Assess the morphology of the erythrocytes.
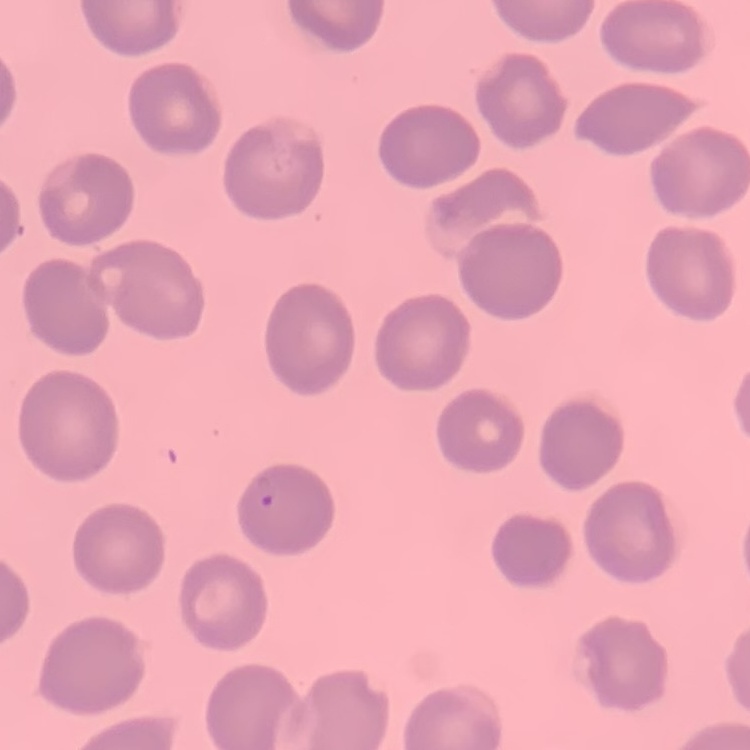
No rouleaux formation.

preparation = thin peripheral smear
image type = one tile cut from a larger photomicrograph
stain = Field's or Giemsa